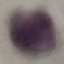

{
  "malaria_status": "uninfected",
  "capture": "smartphone camera at the microscope eyepiece",
  "stain": "Giemsa",
  "image_type": "cell patch, automatically extracted from a larger field of view and resized to 64 × 64 pixels",
  "preparation": "thin blood film"
}